Locate every uninfected red blood cell.
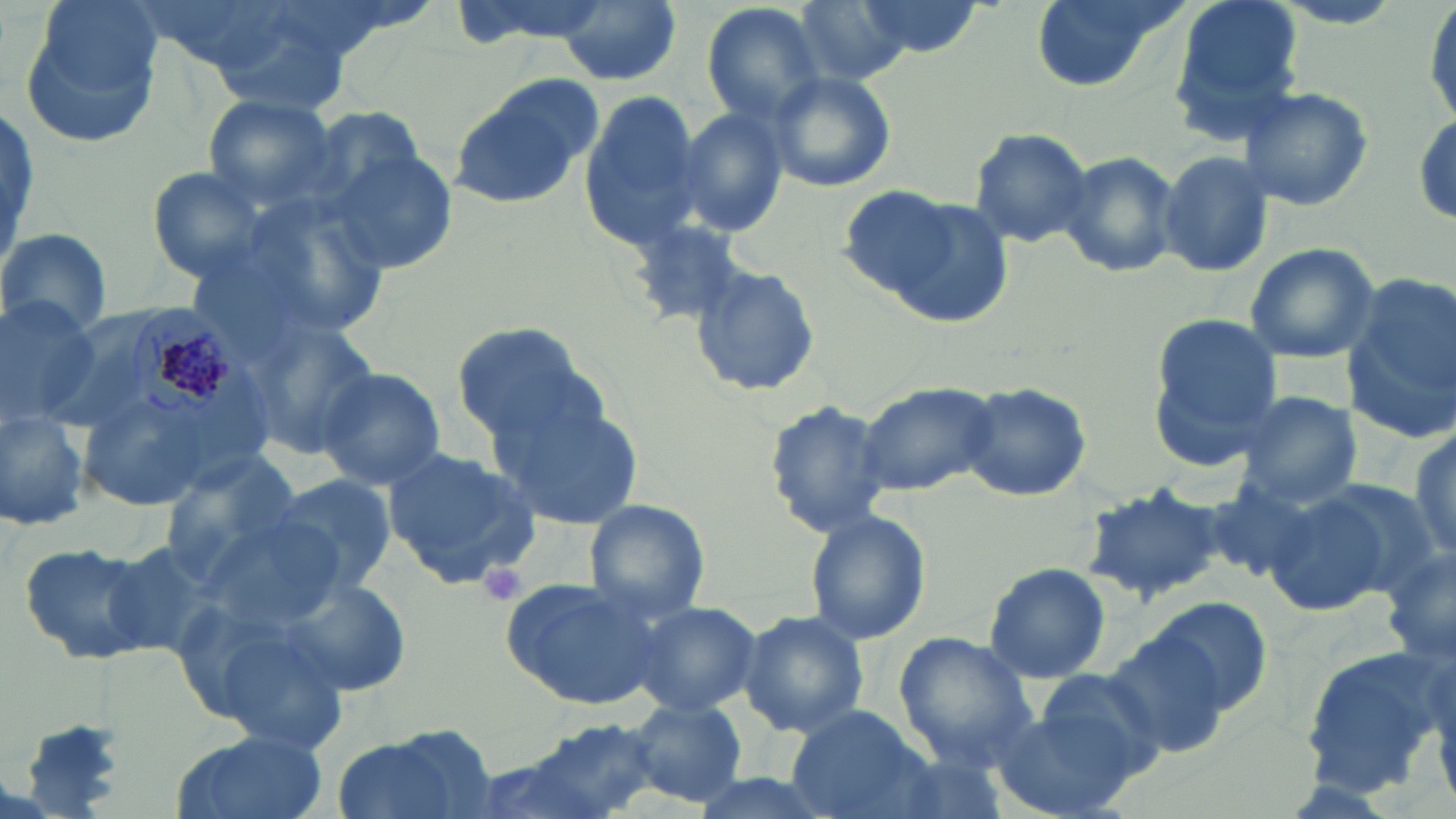

Approximate bounding boxes as (x1, y1, x2, y2) in pixels.
Uninfected red blood cells: (21, 0, 161, 148), (142, 0, 301, 74), (791, 0, 913, 86), (856, 0, 986, 56), (1025, 0, 1189, 95), (1167, 0, 1305, 140), (556, 1, 680, 85), (699, 3, 832, 131), (1423, 3, 1456, 127), (761, 69, 897, 193), (446, 78, 600, 210), (1236, 85, 1375, 211), (578, 94, 707, 253), (201, 95, 336, 208), (1409, 105, 1456, 233), (676, 107, 790, 240), (967, 128, 1095, 248), (1054, 148, 1181, 280), (1158, 149, 1276, 280), (325, 151, 462, 274), (149, 166, 275, 280), (842, 186, 1007, 320), (234, 189, 398, 341), (626, 216, 748, 329), (0, 228, 111, 341), (1241, 242, 1381, 364), (690, 263, 821, 398), (1343, 273, 1455, 441), (0, 296, 104, 427), (1148, 317, 1281, 465), (243, 320, 380, 460), (450, 323, 599, 446), (316, 366, 446, 492), (857, 380, 996, 493), (955, 381, 1094, 503), (491, 391, 641, 527), (77, 392, 220, 509), (1236, 393, 1362, 508), (764, 398, 891, 538), (0, 406, 91, 534), (1407, 420, 1456, 565), (382, 444, 541, 587), (158, 447, 304, 571), (270, 473, 399, 597), (1201, 479, 1320, 583), (1075, 480, 1236, 606), (1261, 486, 1403, 619), (584, 499, 712, 624), (802, 507, 929, 646), (17, 539, 163, 668), (982, 562, 1110, 682), (501, 576, 668, 712), (285, 577, 411, 697), (1144, 595, 1274, 719), (628, 600, 761, 718), (736, 610, 871, 737), (1103, 628, 1247, 759), (892, 635, 1039, 766), (1300, 640, 1446, 794), (1029, 669, 1171, 785), (623, 697, 749, 808), (991, 705, 1142, 818), (786, 706, 932, 819), (522, 718, 670, 816), (330, 726, 500, 819), (170, 730, 331, 819), (458, 751, 615, 819).

plasmodium_malariae_infected_red_blood_cell_locations: 'approximate bounding boxes as (x1, y1, x2, y2) in pixels: (126, 298, 236, 424)'
slide_level_diagnosis: Plasmodium malariae
field_of_view: one of a larger specimen
modality: optical microscopy
stain: May-Grünwald-Giemsa
preparation: thin blood film
image_size: 1456×819 pixels
platelet_locations: 'approximate bounding boxes as (x1, y1, x2, y2) in pixels: (476, 560, 528, 608)'
magnification: 1000x